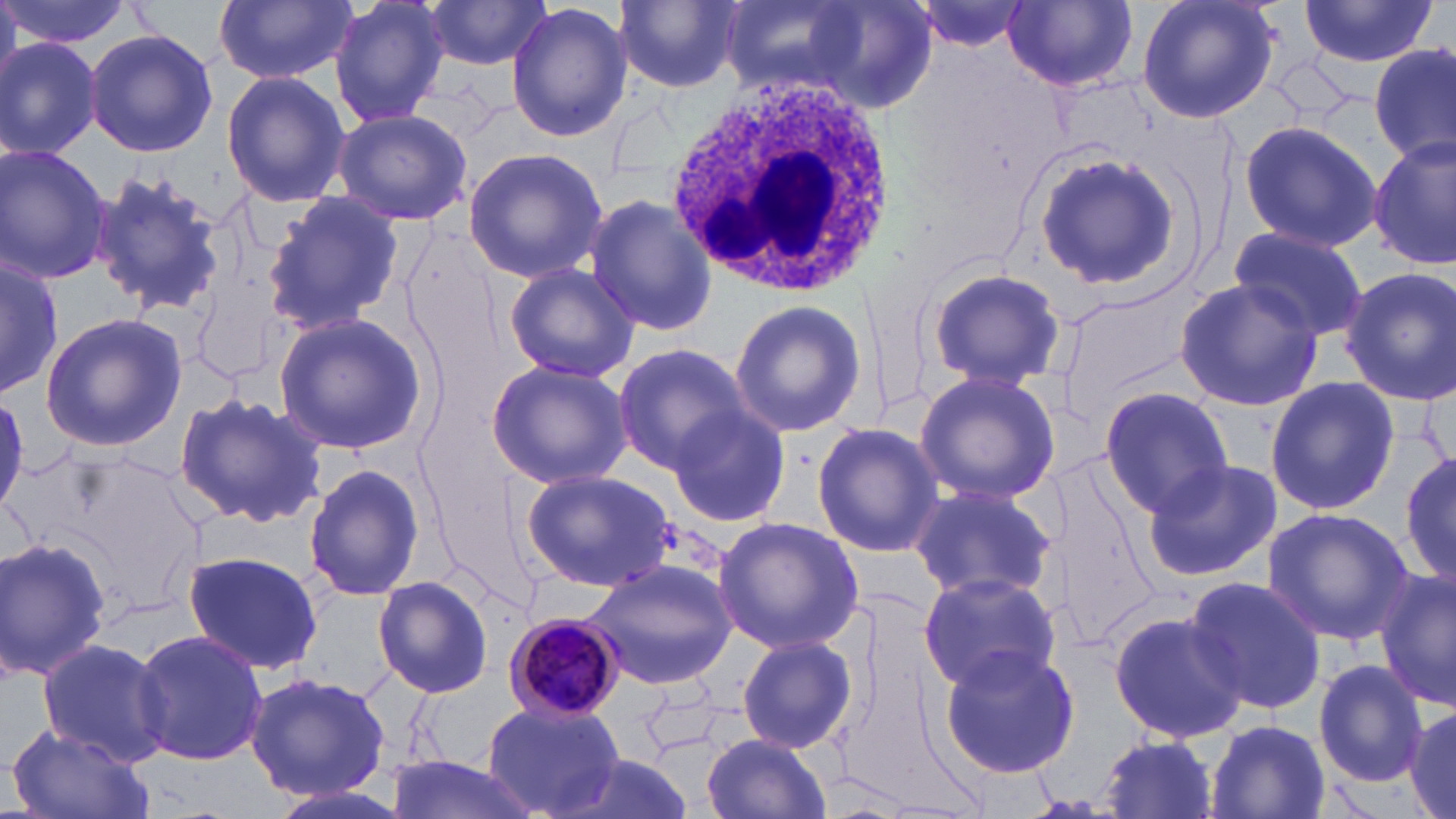
Approximate bounding boxes as (x1, y1, x2, y2) in pixels. Uninfected red blood cell locations: (1, 0, 130, 53), (212, 0, 356, 86), (327, 0, 450, 130), (420, 0, 553, 75), (616, 0, 742, 92), (720, 0, 876, 96), (798, 0, 938, 108), (1136, 0, 1285, 126), (1297, 0, 1437, 71), (911, 1, 1032, 52), (1002, 1, 1138, 91), (506, 3, 633, 142), (83, 29, 218, 158), (0, 37, 103, 159), (1371, 41, 1454, 167), (221, 69, 348, 208), (331, 109, 474, 226), (1238, 115, 1388, 254), (1371, 136, 1454, 271), (0, 145, 112, 285), (1031, 147, 1185, 294), (461, 148, 608, 285), (87, 166, 227, 318), (262, 192, 404, 339), (584, 194, 716, 337), (1228, 225, 1367, 343), (1, 256, 62, 399), (503, 262, 639, 383), (925, 267, 1067, 391), (1341, 267, 1456, 404), (1173, 278, 1321, 413), (1054, 286, 1206, 421), (728, 302, 866, 436), (41, 312, 188, 451), (272, 314, 424, 456), (610, 345, 750, 473), (485, 359, 632, 490), (912, 369, 1063, 504), (1266, 378, 1397, 516), (1098, 386, 1233, 520), (173, 390, 329, 529), (0, 397, 30, 510), (667, 405, 792, 528), (811, 423, 945, 557), (1401, 450, 1456, 587), (1140, 458, 1281, 581), (302, 460, 428, 602), (522, 469, 674, 591), (905, 481, 1058, 604), (1262, 508, 1414, 647), (712, 516, 864, 655), (0, 536, 113, 685), (184, 551, 324, 676), (582, 553, 741, 693), (1375, 566, 1456, 711), (917, 572, 1061, 695), (371, 574, 493, 699), (1185, 574, 1325, 716), (1107, 606, 1250, 744), (133, 630, 268, 765), (736, 635, 855, 753), (35, 636, 170, 766), (937, 640, 1084, 778), (1313, 660, 1428, 785), (245, 670, 391, 804), (480, 700, 626, 818), (1403, 700, 1456, 819), (1208, 719, 1328, 817), (6, 726, 152, 819), (700, 734, 830, 819), (1098, 736, 1219, 818), (384, 757, 547, 819). White blood cell locations: (664, 73, 896, 299). Plasmodium malariae-infected red blood cell locations: (503, 612, 625, 721). Slide-level diagnosis: Plasmodium malariae. Image is 1456×819 pixels. May-Grünwald-Giemsa stain. Optical microscopy. Thin blood smear. 1000x magnification. One field of a larger specimen.